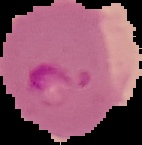 The area outside the segmented cell region is set to black. Malaria status: parasitized. From a thin blood film. Image is 142×145 pixels.